Name the parasite shown.
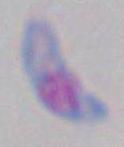

This is Toxoplasma gondii.

Summary:
  - Modality: micrograph
  - Magnification: 1000x